Report the malaria status of this cell.
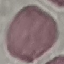
It is uninfected.

Summary:
  - Capture: smartphone camera at the microscope eyepiece
  - Image type: cell patch, automatically extracted from a larger field of view and resized to 64 × 64 pixels
  - Preparation: thin blood film
  - Stain: Giemsa